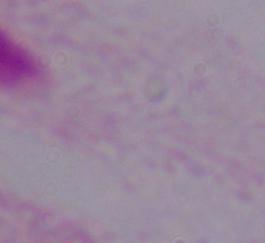

Summary:
  - Modality: photomicrograph
  - Identification: trichomonad
  - Magnification: 1000x